Comment on the morphology of the erythrocytes.
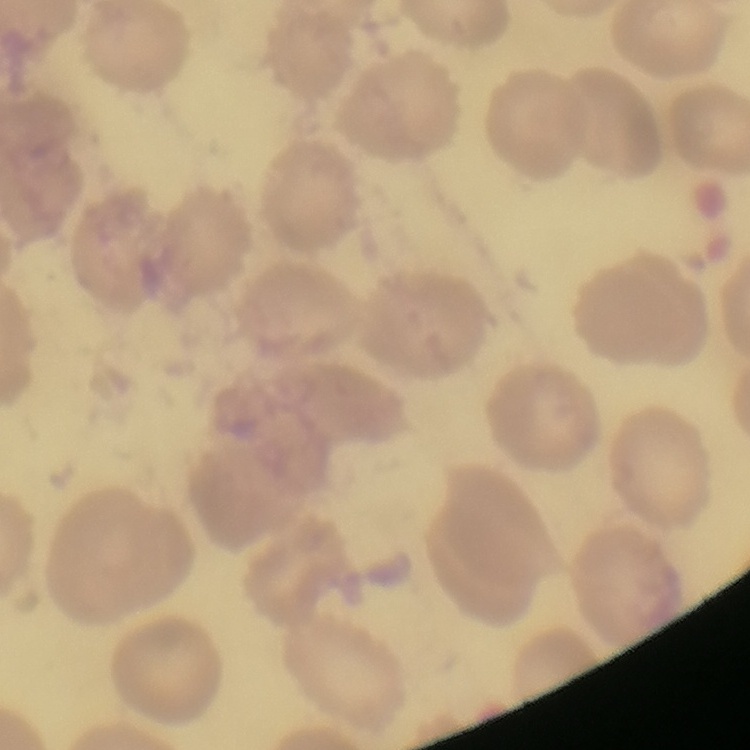

No rouleaux formation.

image type = square crop of a larger photomicrograph
stain = Field's or Giemsa
preparation = thin peripheral smear